Give the preparation type.
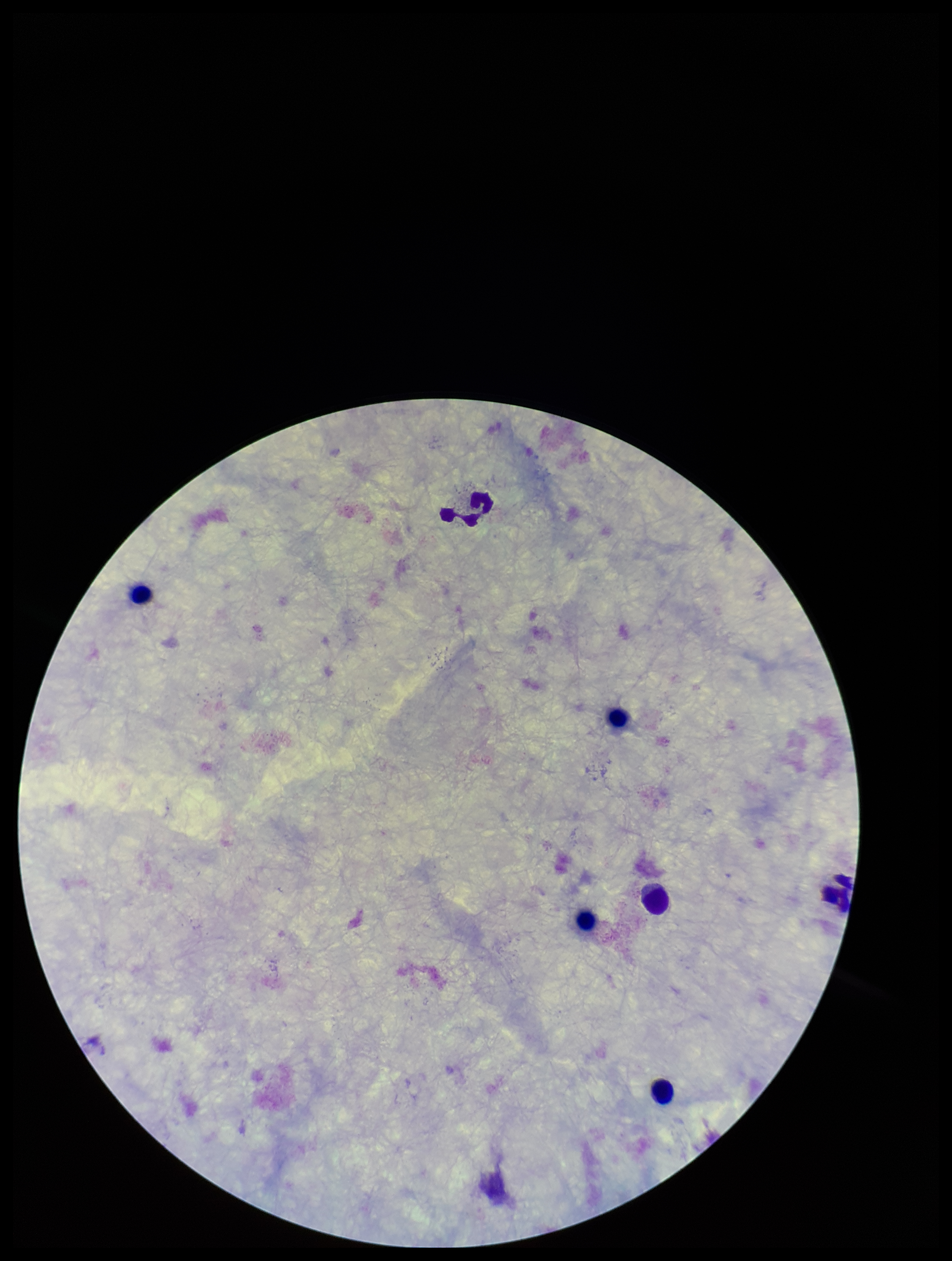

A thick smear.

parasite count = 0
Plasmodium parasites = none seen
leukocyte count = 7
patient malaria status = negative
stain = Giemsa
field of view = single
capture = smartphone photograph through the microscope eyepiece
image size = 952×1261 pixels